Name the blood parasite species.
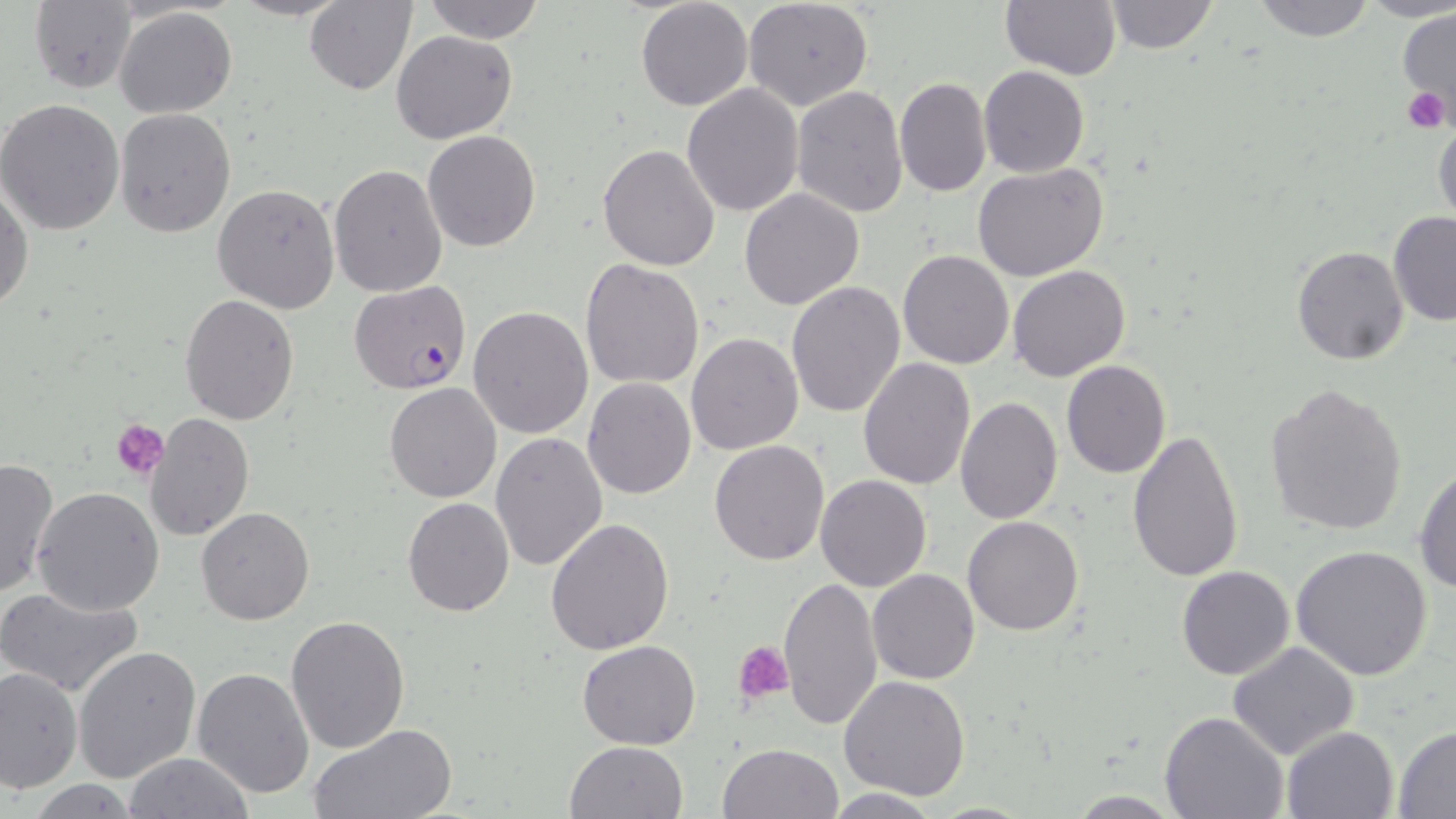
Plasmodium falciparum.

Summary:
  - Coordinate format: approximate bounding boxes as (x1, y1, x2, y2) in pixels
  - Uninfected red blood cell locations: (304, 0, 416, 95), (420, 0, 547, 43), (636, 0, 753, 112), (1251, 0, 1378, 41), (742, 1, 874, 111), (1000, 1, 1122, 79), (1101, 1, 1218, 54), (29, 2, 138, 93), (115, 6, 237, 117), (1397, 7, 1456, 117), (641, 9, 865, 148), (392, 29, 518, 145), (979, 65, 1089, 178), (895, 76, 990, 196), (680, 83, 804, 215), (791, 86, 908, 218), (0, 98, 126, 236), (114, 109, 236, 239), (1431, 115, 1455, 231), (422, 131, 541, 252), (598, 144, 721, 271), (973, 162, 1110, 282), (328, 164, 448, 298), (0, 172, 33, 317), (213, 184, 340, 313), (739, 188, 867, 311), (1387, 211, 1456, 327), (1292, 245, 1411, 366), (897, 249, 1014, 369), (579, 258, 706, 391), (1006, 265, 1131, 382), (786, 282, 906, 418), (179, 294, 301, 426), (468, 306, 594, 439), (686, 332, 804, 456), (858, 357, 975, 489), (1060, 359, 1171, 477), (582, 377, 697, 499), (1264, 380, 1409, 536), (386, 382, 501, 502), (954, 396, 1062, 523), (145, 412, 255, 542), (1128, 430, 1246, 584), (491, 433, 608, 572), (710, 440, 829, 566), (0, 456, 59, 599), (1414, 465, 1456, 594), (814, 475, 931, 592), (32, 486, 165, 615), (402, 497, 514, 618), (196, 506, 313, 625), (545, 516, 675, 656), (962, 516, 1083, 636), (1290, 544, 1434, 680), (1175, 566, 1294, 681), (867, 568, 980, 684), (777, 576, 884, 730), (0, 586, 145, 698), (285, 615, 410, 754), (577, 640, 702, 749), (1228, 640, 1360, 760), (73, 645, 201, 783), (1, 664, 82, 793), (191, 666, 315, 801), (838, 675, 970, 801), (1160, 711, 1288, 819), (308, 724, 458, 818), (1282, 725, 1399, 818), (1392, 728, 1456, 815), (565, 740, 690, 819), (718, 742, 841, 819), (121, 753, 258, 818), (820, 788, 947, 817)
  - Plasmodium falciparum-infected red blood cell locations: (349, 280, 472, 395)
  - Platelet locations: (1403, 88, 1450, 133), (113, 420, 170, 482), (735, 641, 794, 704)
  - Magnification: 1000x
  - Modality: optical microscopy
  - Preparation: thin blood smear
  - Stain: May-Grünwald-Giemsa
  - Image size: 1456×819 pixels
  - Field of view: one of a larger specimen